Name the cell type shown.
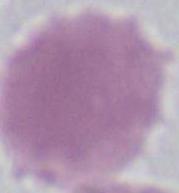

An erythrocyte.

magnification = 1000x
modality = photomicrograph